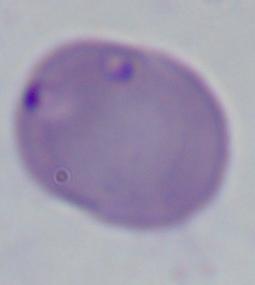

magnification = 1000x
identification = Babesia
modality = micrograph